Name the parasite shown.
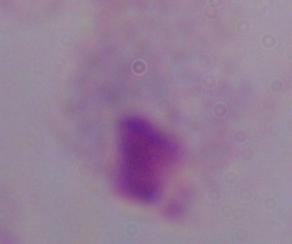

A trichomonad.

modality = micrograph
magnification = 1000x